Describe the morphology of the erythrocytes.
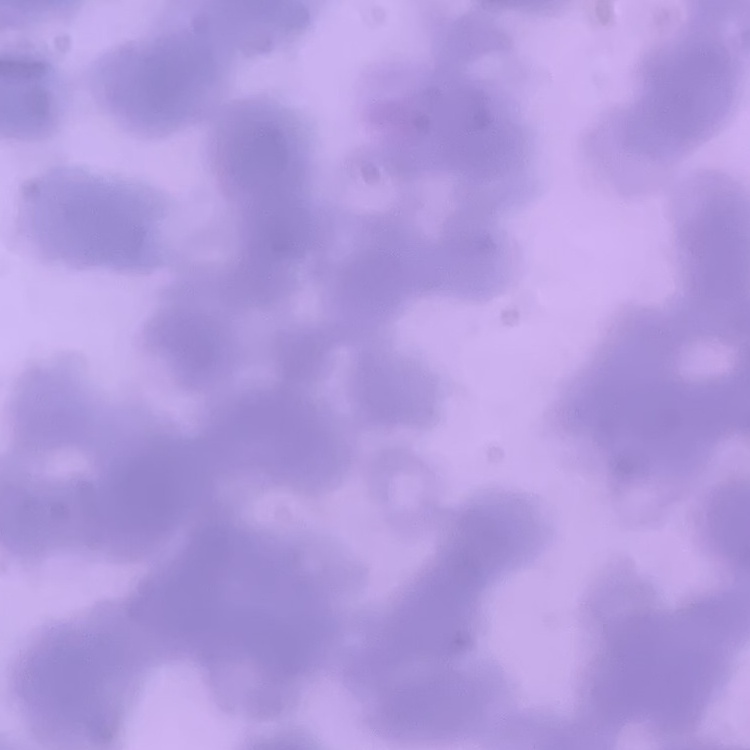

They show rouleaux formation.

stain = Field's or Giemsa
preparation = thin peripheral smear
image type = one tile cut from a larger photomicrograph